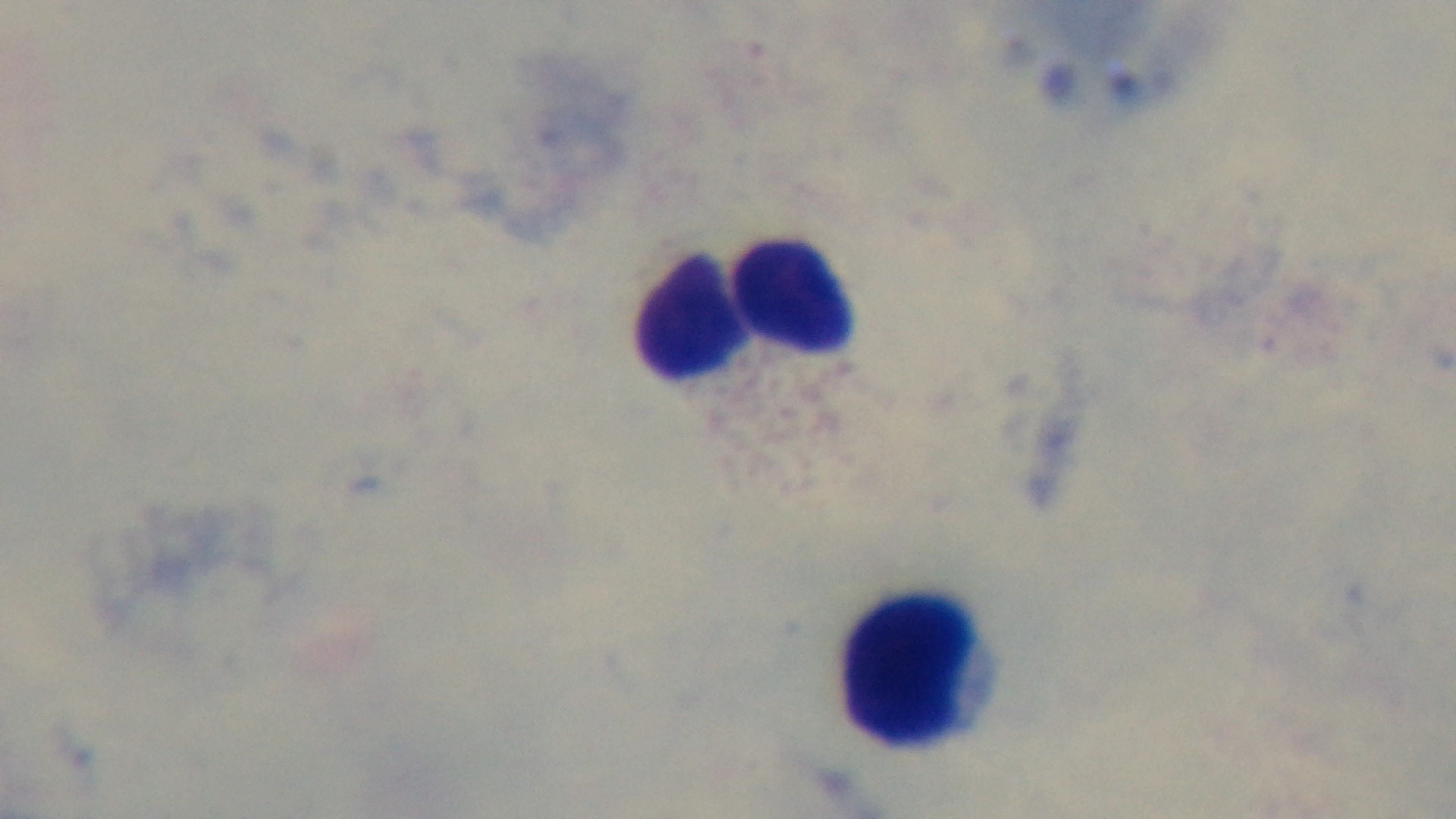
Summary:
  - Modality: light microscopy
  - Preparation: thick
  - Malaria status: uninfected
  - Field of view: one from the slide
  - Capture: mounted 4K digital camera
  - Stain: Giemsa
  - Objective: 100x oil immersion